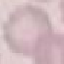
Summary:
  - Malaria status: uninfected
  - Image type: cell patch, automatically extracted from a larger field of view and resized to 64 × 64 pixels
  - Preparation: thin smear
  - Capture: smartphone camera at the microscope eyepiece
  - Stain: Giemsa